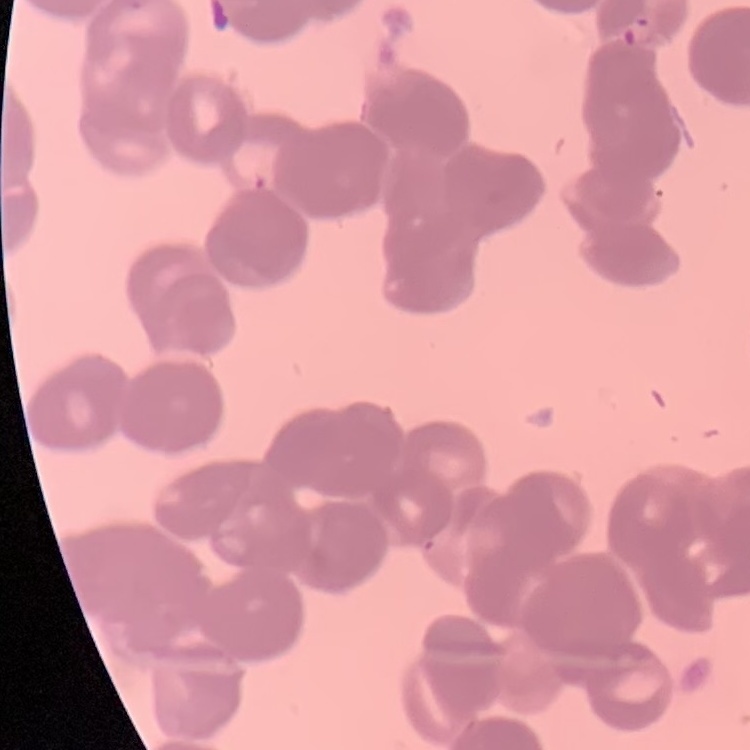
Summary:
  - Red blood cell morphology: rouleaux formation
  - Stain: Field's or Giemsa
  - Image type: one tile cut from a larger photomicrograph
  - Preparation: thin peripheral smear